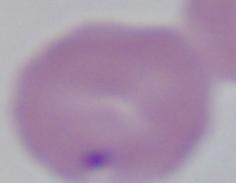

Summary:
  - Modality: photomicrograph
  - Identification: Babesia
  - Magnification: 1000x